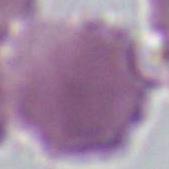
1000x magnification. Micrograph. An erythrocyte is shown.